Locate every Plasmodium falciparum-infected red blood cell.
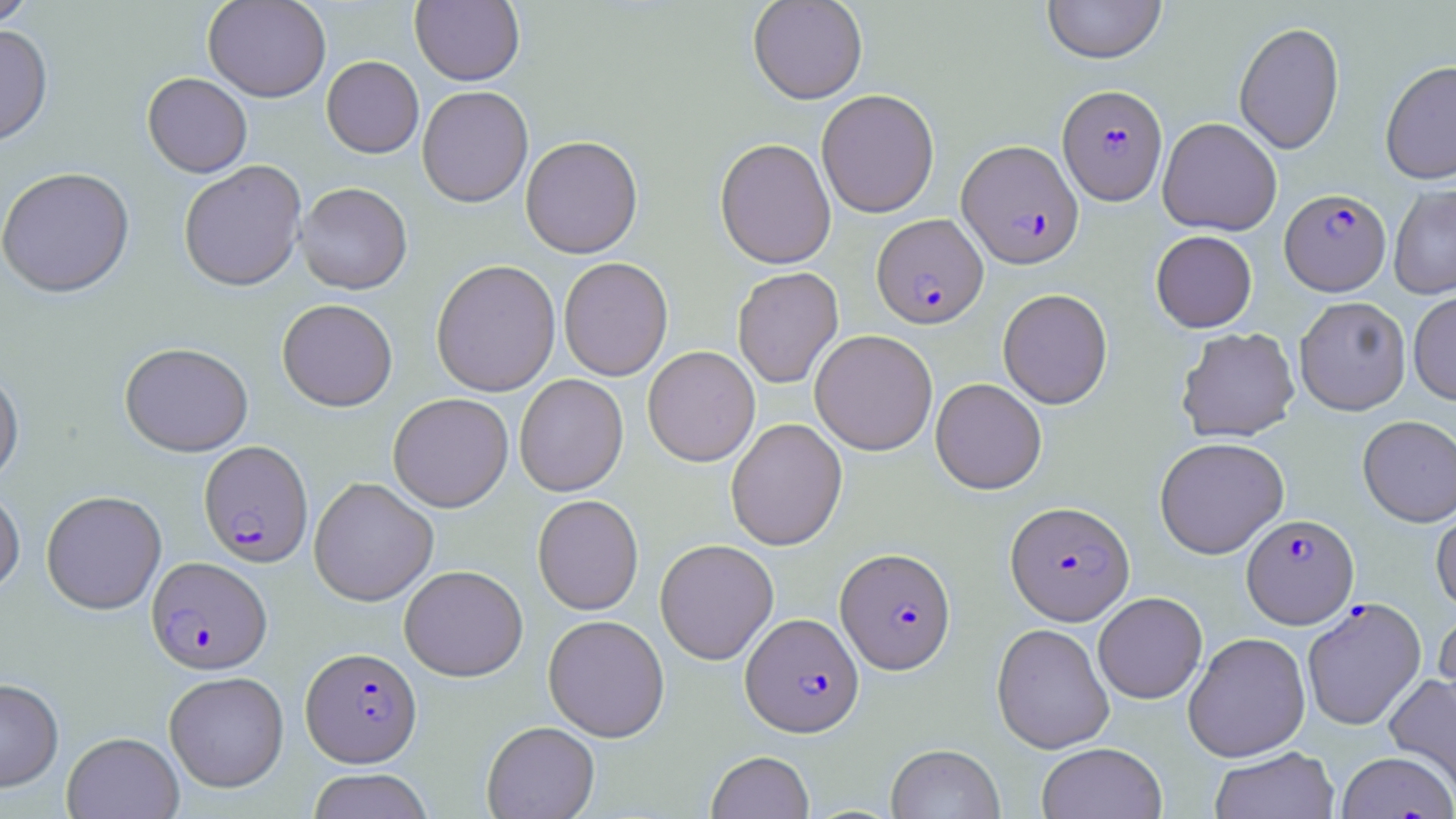

Approximate bounding boxes as (x1,y1)-(x2,y2) corner pairs in pixels.
Plasmodium falciparum-infected red blood cells: (1058,84)-(1168,205), (957,139)-(1083,269), (1280,188)-(1390,296), (871,213)-(988,327), (199,440)-(314,567), (1005,500)-(1134,625), (1241,514)-(1359,629), (836,547)-(956,673), (146,556)-(271,674), (1302,597)-(1427,730), (741,612)-(863,737), (301,646)-(421,766), (1336,751)-(1456,819).

Uninfected red blood cell locations: (0,0)-(38,30), (203,0)-(331,102), (410,0)-(525,86), (748,0)-(868,104), (1042,0)-(1167,64), (1233,21)-(1345,155), (0,24)-(53,147), (321,55)-(424,158), (1380,60)-(1456,184), (142,72)-(252,177), (417,85)-(533,207), (816,89)-(939,218), (1158,117)-(1282,235), (520,135)-(643,258), (715,137)-(836,269), (178,159)-(307,292), (0,167)-(135,298), (296,182)-(413,294), (1388,183)-(1456,299), (1151,230)-(1257,332), (558,257)-(673,381), (431,259)-(561,397), (732,267)-(843,388), (997,288)-(1113,408), (1408,292)-(1456,405), (1294,296)-(1411,415), (277,298)-(398,411), (1176,327)-(1300,442), (810,329)-(937,455), (120,342)-(253,456), (642,346)-(760,466), (0,367)-(24,487), (514,373)-(629,496), (930,377)-(1047,494), (387,393)-(513,512), (1357,415)-(1456,526), (726,418)-(848,550), (1154,436)-(1289,559), (309,476)-(439,606), (0,485)-(25,597), (41,490)-(167,614), (532,494)-(643,615), (1431,507)-(1456,613), (655,538)-(779,664), (399,564)-(528,681), (1093,592)-(1208,704), (1434,609)-(1456,726), (543,614)-(670,742), (991,622)-(1114,754), (1183,631)-(1311,762), (163,671)-(289,792), (1383,674)-(1456,795), (0,678)-(64,793), (481,721)-(600,819), (62,732)-(183,819), (1036,742)-(1167,819), (886,743)-(1004,819), (1209,746)-(1340,819), (706,751)-(815,819), (308,769)-(433,819). Slide-level diagnosis: Plasmodium falciparum. May-Grünwald-Giemsa stain. Optical microscopy. Image is 1456×819 pixels. 1000x magnification. Thin blood smear. One field of a larger specimen.